Classify this cell by malaria status.
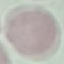
Uninfected.

capture = smartphone through the microscope eyepiece
preparation = thin blood film
stain = Giemsa
image type = automatically extracted cell patch, resized to 64 × 64 pixels